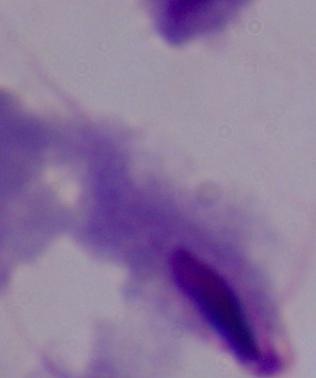

identification = trichomonad
modality = micrograph
magnification = 1000x